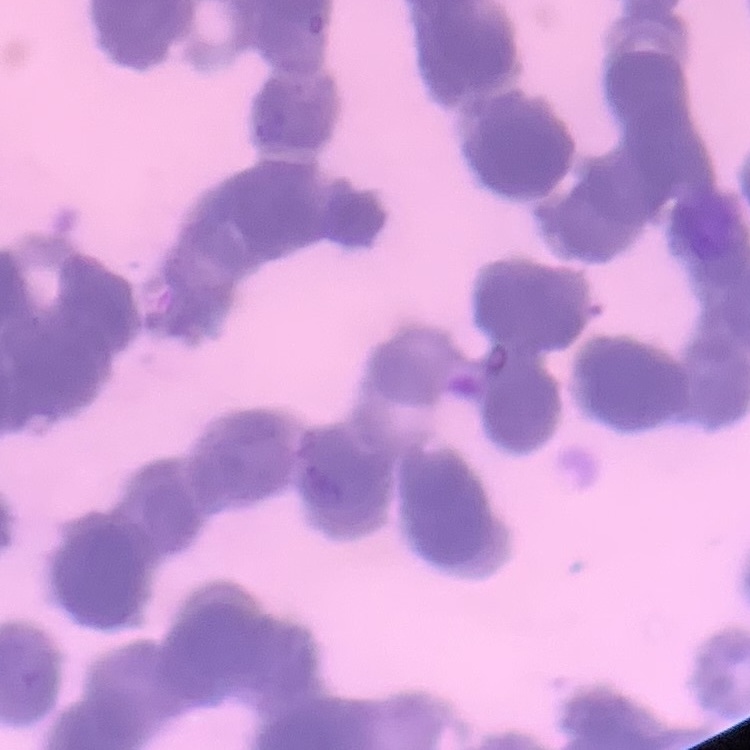
Summary:
  - Erythrocyte morphology: rouleaux formation
  - Image type: square crop of a larger photomicrograph
  - Stain: Field's or Giemsa
  - Preparation: thin peripheral smear